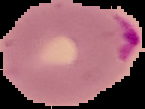

Summary:
  - Malaria status: parasitized
  - Image size: 145×109 pixels
  - Preparation: thin blood smear
  - Image type: segmented cell region on a black background